Assess the morphology of the erythrocytes.
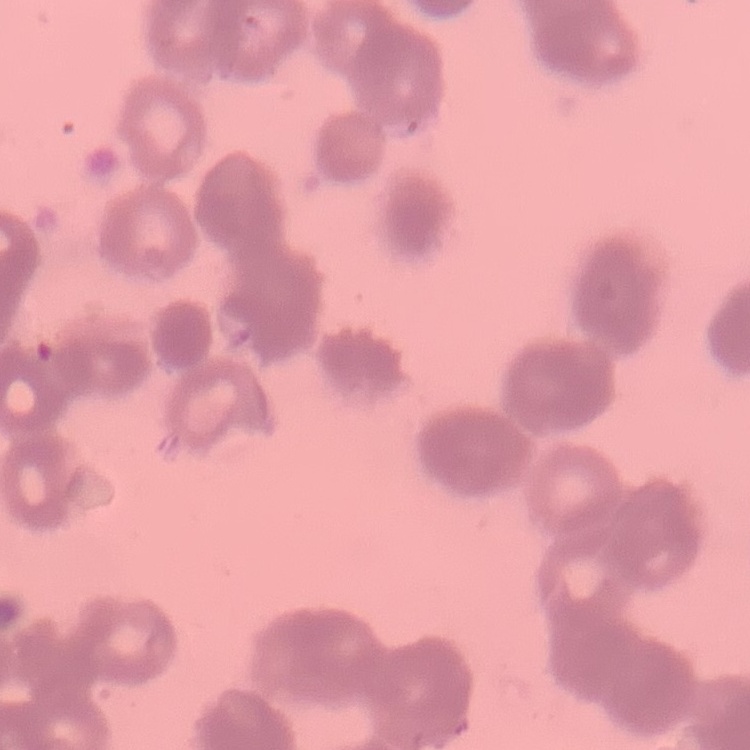

Rouleaux formation.

image type = one tile cut from a larger photomicrograph
preparation = thin peripheral smear
stain = Field's or Giemsa